Assess the morphology of the erythrocytes.
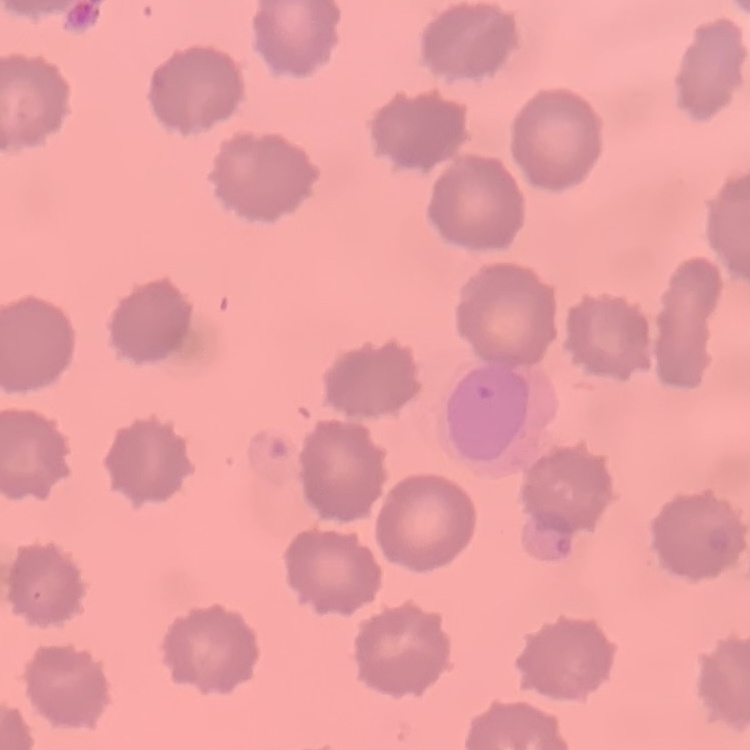

They show no rouleaux formation.

One tile cut from a larger photomicrograph. Stained with either Field's or Giemsa. Thin blood film.